Classify this cell by malaria status.
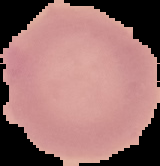
It is uninfected.

Segmented cell region on a black background. Image is 160×166 pixels. From a thin blood film.